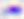

400x magnification. Photomicrograph. Toxoplasma gondii is seen.